Give the position of every leukocyte visible.
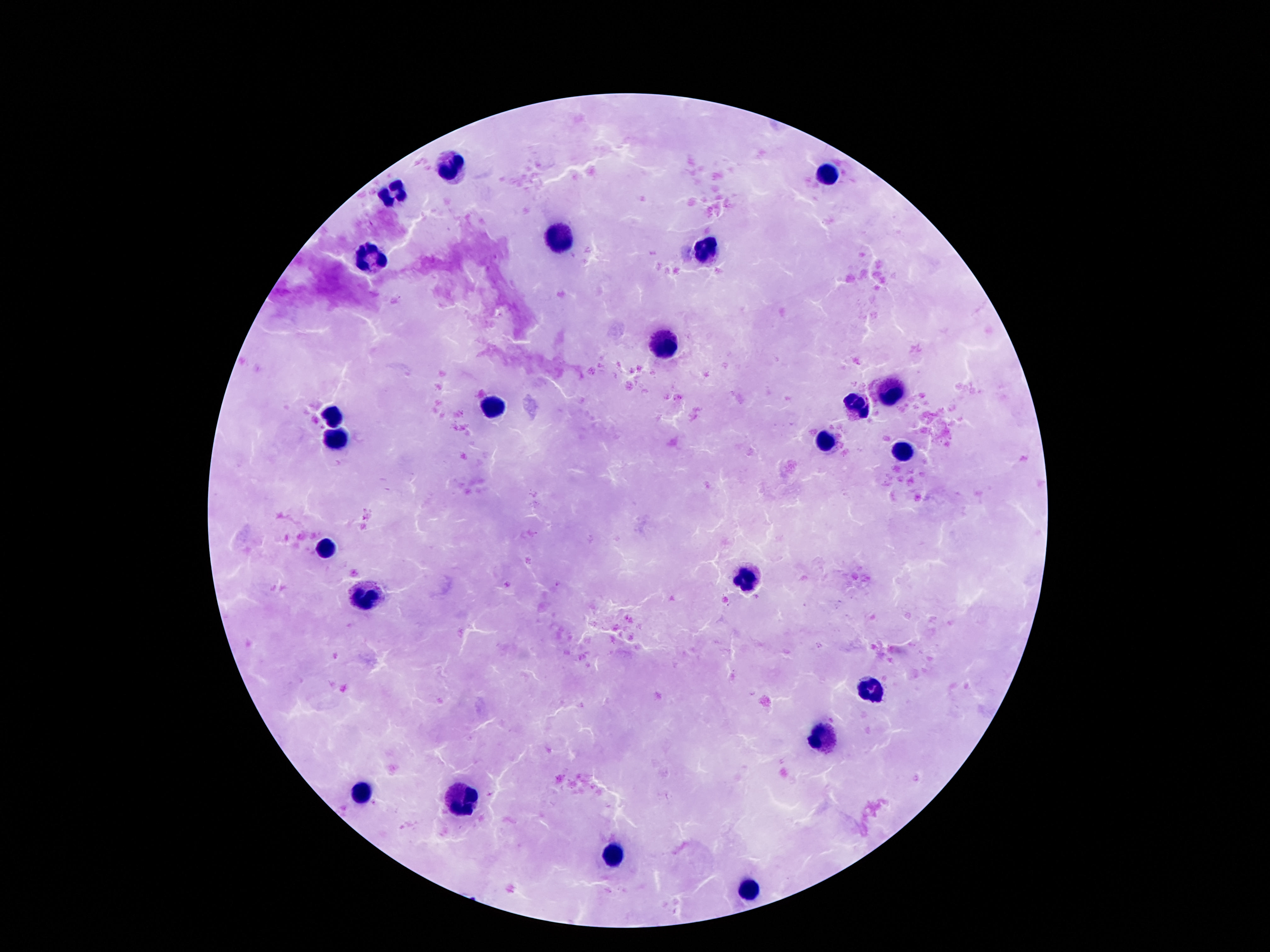
Approximate object centers, in pixels from the top-left corner.
Leukocytes: (x=452, y=165), (x=829, y=176), (x=395, y=189), (x=558, y=237), (x=706, y=249), (x=372, y=258), (x=661, y=344), (x=888, y=391), (x=851, y=407), (x=491, y=408), (x=331, y=417), (x=335, y=436), (x=827, y=440), (x=900, y=452), (x=325, y=552), (x=747, y=580), (x=366, y=598), (x=872, y=690), (x=823, y=735), (x=360, y=794), (x=464, y=801), (x=608, y=856), (x=745, y=888).

Summary:
  - Stain: Giemsa
  - Preparation: thick peripheral-blood smear
  - Image size: 1270×952 pixels
  - Capture: smartphone camera through the microscope eyepiece
  - Field of view: one from this slide
  - Patient malaria status: not infected
  - Magnification: 100x